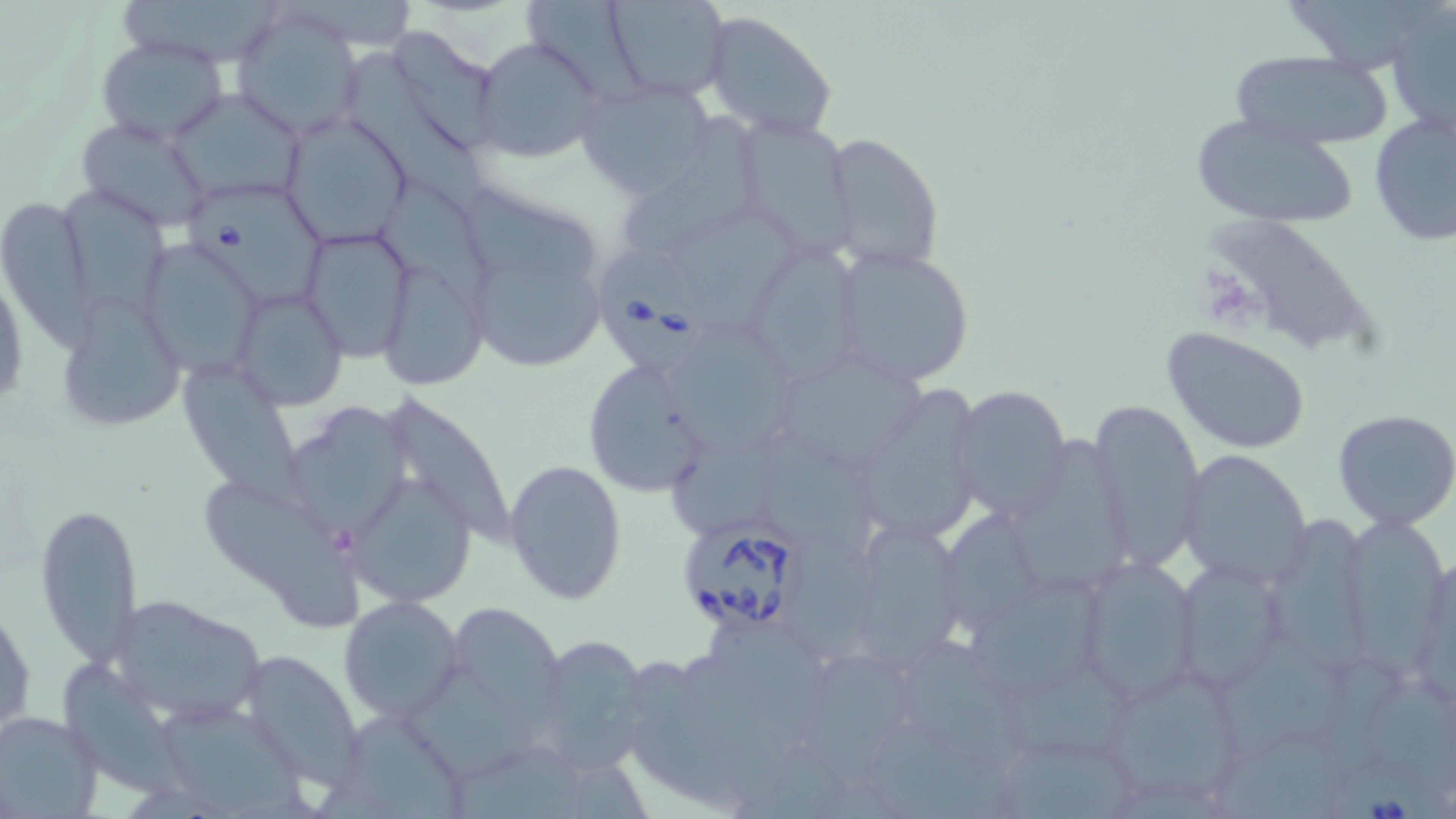

Approximate bounding boxes as named x1/y1/x2/y2 corners in pixels. Uninfected red blood cell locations: (x1=606, y1=0, x2=731, y2=102), (x1=1291, y1=0, x2=1448, y2=70), (x1=522, y1=1, x2=653, y2=111), (x1=123, y1=2, x2=284, y2=63), (x1=1387, y1=6, x2=1455, y2=135), (x1=228, y1=7, x2=366, y2=140), (x1=703, y1=13, x2=837, y2=138), (x1=400, y1=29, x2=501, y2=148), (x1=472, y1=34, x2=604, y2=162), (x1=96, y1=36, x2=229, y2=146), (x1=1226, y1=49, x2=1396, y2=151), (x1=349, y1=51, x2=494, y2=218), (x1=575, y1=80, x2=717, y2=200), (x1=168, y1=88, x2=305, y2=203), (x1=1369, y1=110, x2=1456, y2=248), (x1=625, y1=112, x2=760, y2=257), (x1=279, y1=114, x2=411, y2=247), (x1=1187, y1=115, x2=1360, y2=229), (x1=734, y1=116, x2=852, y2=254), (x1=76, y1=117, x2=215, y2=232), (x1=823, y1=133, x2=945, y2=273), (x1=376, y1=181, x2=508, y2=318), (x1=60, y1=183, x2=168, y2=319), (x1=467, y1=188, x2=602, y2=287), (x1=0, y1=196, x2=94, y2=351), (x1=669, y1=216, x2=798, y2=335), (x1=1217, y1=220, x2=1380, y2=353), (x1=300, y1=227, x2=416, y2=361), (x1=739, y1=243, x2=864, y2=381), (x1=828, y1=245, x2=975, y2=387), (x1=150, y1=246, x2=264, y2=377), (x1=383, y1=265, x2=485, y2=388), (x1=474, y1=265, x2=605, y2=369), (x1=234, y1=291, x2=347, y2=412), (x1=67, y1=298, x2=186, y2=429), (x1=669, y1=327, x2=810, y2=454), (x1=1163, y1=328, x2=1311, y2=455), (x1=582, y1=362, x2=705, y2=497), (x1=782, y1=362, x2=929, y2=472), (x1=180, y1=374, x2=320, y2=518), (x1=951, y1=385, x2=1071, y2=522), (x1=866, y1=387, x2=986, y2=541), (x1=384, y1=390, x2=532, y2=548), (x1=1089, y1=398, x2=1205, y2=575), (x1=285, y1=403, x2=413, y2=541), (x1=1332, y1=409, x2=1456, y2=530), (x1=765, y1=422, x2=894, y2=567), (x1=671, y1=432, x2=784, y2=539), (x1=1177, y1=451, x2=1312, y2=588), (x1=505, y1=458, x2=629, y2=604), (x1=201, y1=480, x2=372, y2=627), (x1=349, y1=481, x2=486, y2=604), (x1=35, y1=498, x2=142, y2=671), (x1=1351, y1=512, x2=1449, y2=683), (x1=942, y1=513, x2=1045, y2=644), (x1=1276, y1=517, x2=1373, y2=681), (x1=855, y1=528, x2=963, y2=669), (x1=1413, y1=552, x2=1456, y2=713), (x1=1073, y1=553, x2=1205, y2=705), (x1=1181, y1=560, x2=1281, y2=686), (x1=973, y1=581, x2=1110, y2=698), (x1=104, y1=594, x2=267, y2=725), (x1=1, y1=595, x2=35, y2=745), (x1=338, y1=595, x2=466, y2=724), (x1=445, y1=604, x2=584, y2=743), (x1=708, y1=624, x2=825, y2=757), (x1=1219, y1=627, x2=1357, y2=761), (x1=525, y1=633, x2=652, y2=773), (x1=907, y1=637, x2=1019, y2=769), (x1=792, y1=651, x2=913, y2=793), (x1=241, y1=652, x2=365, y2=790), (x1=1013, y1=658, x2=1144, y2=757), (x1=630, y1=659, x2=754, y2=811), (x1=1093, y1=661, x2=1251, y2=809), (x1=408, y1=665, x2=548, y2=778), (x1=61, y1=666, x2=182, y2=799), (x1=1371, y1=682, x2=1456, y2=792), (x1=164, y1=707, x2=311, y2=819), (x1=0, y1=710, x2=105, y2=819), (x1=352, y1=714, x2=467, y2=819), (x1=449, y1=736, x2=596, y2=819), (x1=1215, y1=737, x2=1357, y2=819), (x1=1007, y1=741, x2=1131, y2=819). Platelet locations: (x1=1198, y1=268, x2=1258, y2=326). Babesia divergens-infected red blood cell locations: (x1=189, y1=186, x2=335, y2=313), (x1=597, y1=256, x2=717, y2=373), (x1=682, y1=521, x2=806, y2=638), (x1=1325, y1=751, x2=1455, y2=819). Slide-level diagnosis: Babesia divergens. Light microscopy. One field of a larger specimen. Image is 1456×819 pixels. Thin blood film. Captured at 1000x magnification. May-Grünwald-Giemsa stain.